Point out each leukocyte.
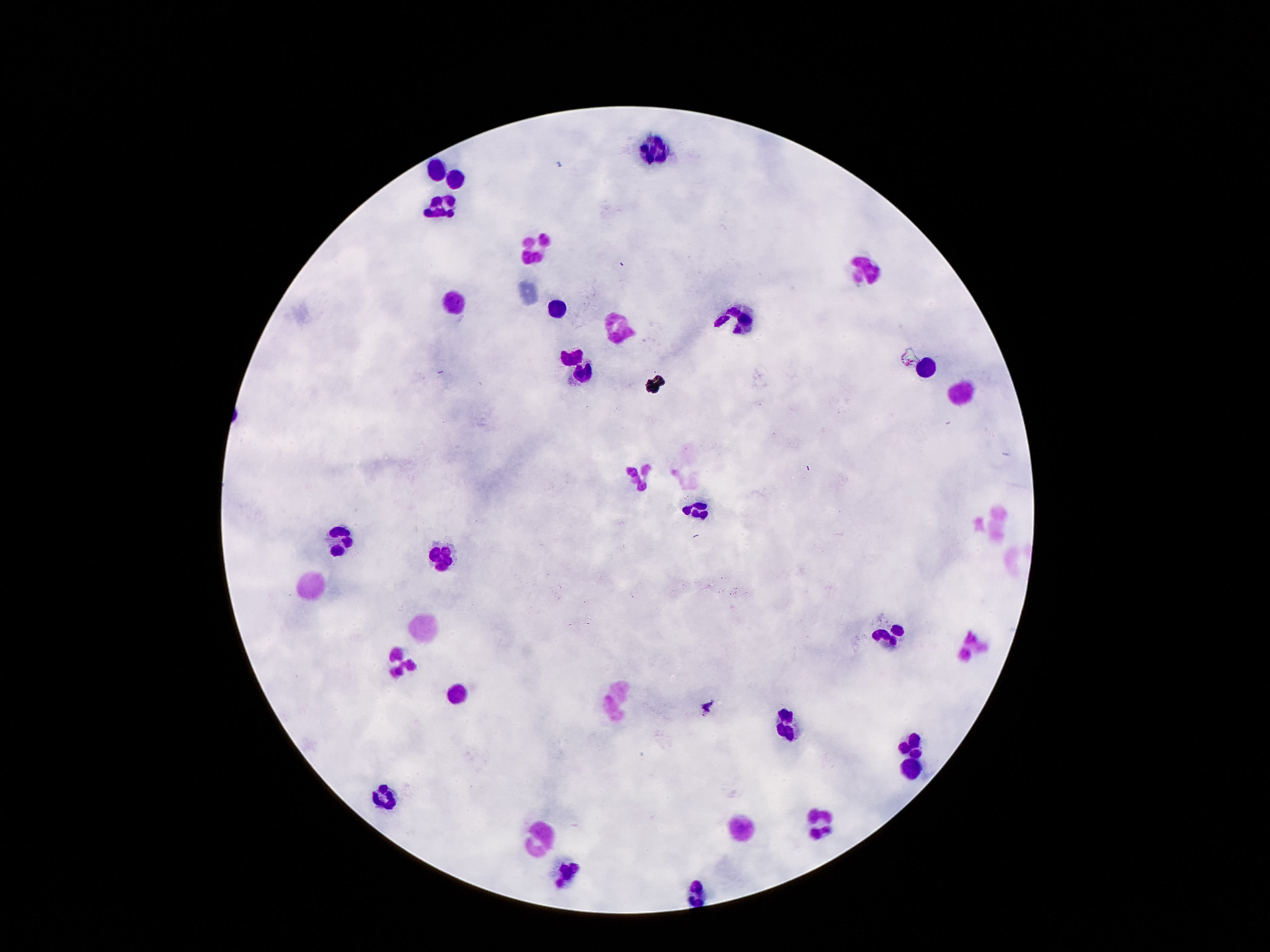

Approximate centers as (x, y) in pixels.
Leukocytes: (655, 153), (435, 169), (453, 180), (443, 207), (535, 249), (867, 269), (455, 301), (557, 311), (737, 318), (615, 326), (571, 354), (925, 364), (581, 368), (963, 394), (641, 476), (699, 508), (997, 524), (341, 540), (441, 558), (309, 586), (423, 627), (889, 635), (977, 646), (403, 662), (455, 693), (617, 699), (785, 724), (911, 749), (913, 770), (385, 797), (819, 823), (739, 829), (541, 838), (565, 871), (695, 895).

Giemsa stain. Thick blood smear. Image is 1270×952 pixels. Photographed through the microscope eyepiece with a smartphone camera. Single field of view. Patient malaria status: negative. 100x magnification.